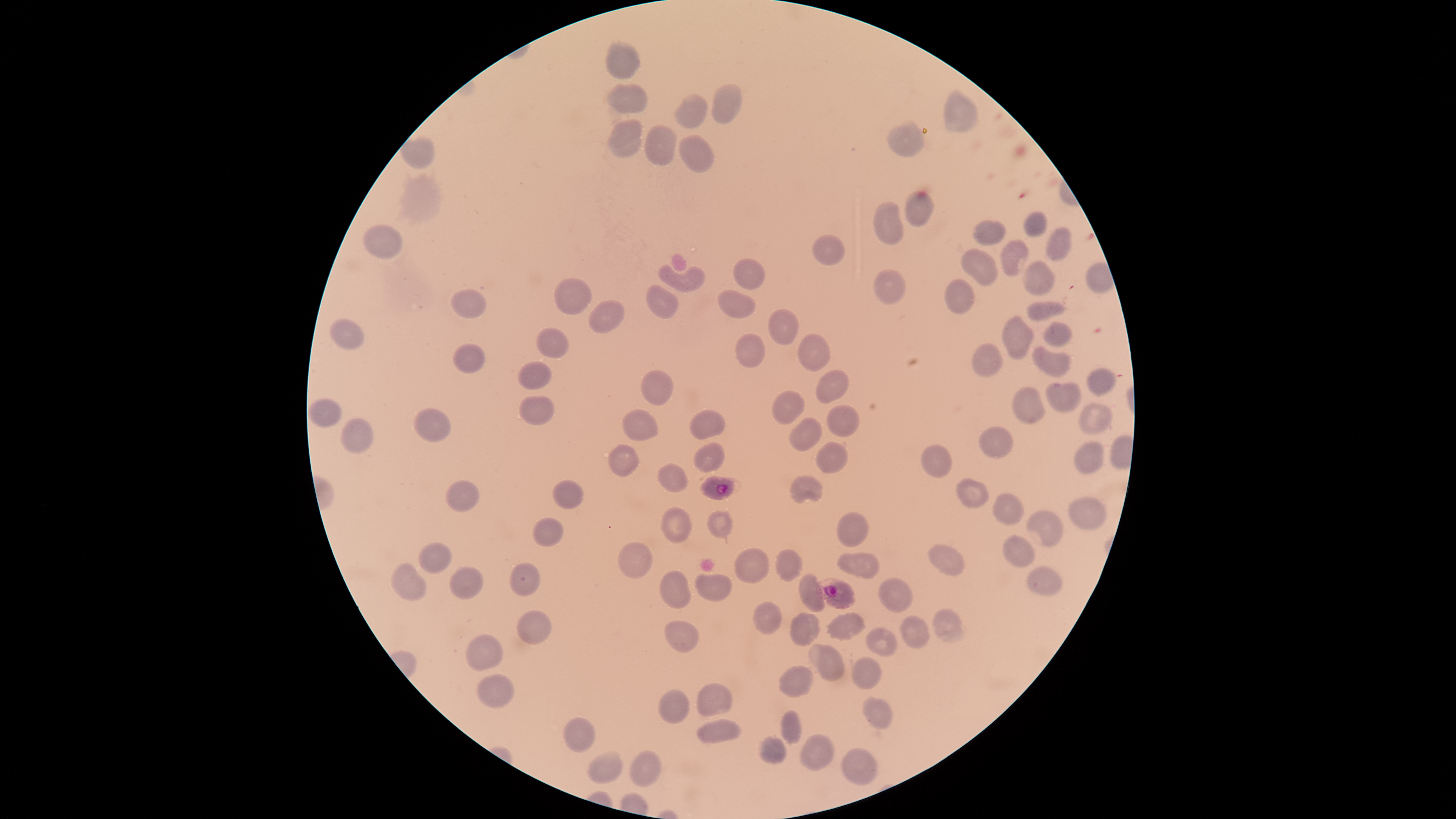

{
  "presence": "malaria parasites identified",
  "capture": "smartphone photograph through the microscope eyepiece",
  "image_size": "1456×819 pixels",
  "parasitized_RBCs": "approximate bounding boxes as {left, top, right, bottom} in pixels: {700, 476, 740, 500}, {815, 578, 855, 609}",
  "preparation": "thin smear of blood",
  "stain": "Giemsa",
  "species": "Plasmodium falciparum",
  "uninfected_RBCs": "approximate bounding boxes as {left, top, right, bottom} in pixels: {605, 39, 641, 78}, {607, 83, 649, 114}, {711, 83, 742, 125}, {944, 88, 979, 132}, {674, 94, 709, 129}, {607, 118, 644, 157}, {887, 120, 925, 158}, {644, 124, 676, 166}, {678, 134, 714, 174}, {399, 135, 436, 169}, {904, 190, 935, 227}, {872, 201, 905, 246}, {1023, 211, 1048, 238}, {972, 219, 1006, 246}, {361, 225, 404, 259}, {1045, 226, 1072, 261}, {811, 233, 847, 266}, {999, 238, 1028, 277}, {960, 247, 998, 288}, {732, 257, 767, 290}, {1022, 259, 1057, 296}, {657, 263, 706, 292}, {873, 269, 907, 305}, {553, 277, 592, 316}, {943, 278, 975, 314}, {645, 283, 679, 319}, {451, 289, 488, 318}, {716, 289, 757, 319}, {587, 299, 626, 334}, {1026, 300, 1068, 321}, {767, 308, 799, 346}, {1001, 314, 1035, 360}, {328, 318, 365, 350}, {1041, 321, 1072, 347}, {536, 326, 571, 359}, {734, 332, 766, 369}, {797, 332, 831, 372}, {971, 342, 1004, 377}, {452, 343, 486, 374}, {1031, 345, 1072, 377}, {517, 360, 551, 390}, {1087, 366, 1117, 397}, {641, 368, 674, 406}, {816, 370, 850, 405}, {1044, 381, 1081, 414}, {1011, 386, 1046, 424}, {771, 390, 805, 425}, {518, 395, 556, 426}, {308, 398, 342, 428}, {1077, 402, 1114, 436}, {826, 404, 861, 438}, {621, 407, 658, 442}, {413, 408, 453, 442}, {689, 409, 726, 440}, {788, 416, 823, 453}, {341, 418, 374, 454}, {977, 425, 1014, 459}, {815, 441, 848, 474}, {1074, 441, 1104, 473}, {692, 442, 725, 473}, {608, 443, 640, 477}, {920, 443, 953, 478}, {656, 462, 689, 493}, {790, 474, 824, 504}, {552, 477, 585, 509}, {955, 477, 990, 509}, {445, 479, 480, 512}, {992, 491, 1026, 525}, {1067, 496, 1109, 530}, {660, 505, 693, 545}, {706, 509, 733, 544}, {1026, 510, 1063, 546}, {836, 511, 870, 548}, {531, 516, 564, 547}, {1002, 534, 1036, 568}, {617, 541, 653, 579}, {417, 542, 453, 575}, {927, 543, 966, 575}, {734, 546, 770, 584}, {775, 548, 804, 582}, {837, 552, 881, 580}, {509, 561, 541, 597}, {390, 562, 427, 602}, {448, 566, 484, 600}, {1026, 566, 1063, 596}, {658, 570, 692, 610}, {797, 571, 826, 612}, {694, 572, 732, 602}, {878, 576, 912, 613}, {751, 600, 783, 635}, {931, 607, 965, 643}, {515, 608, 552, 646}, {789, 611, 822, 647}, {825, 611, 866, 641}, {898, 614, 930, 648}, {664, 619, 700, 653}, {865, 626, 898, 657}, {465, 633, 504, 673}, {808, 643, 845, 682}, {850, 656, 882, 691}, {778, 663, 814, 698}, {476, 674, 515, 709}, {696, 682, 733, 718}, {657, 689, 690, 725}, {864, 695, 894, 730}, {778, 709, 802, 746}, {563, 716, 596, 754}, {695, 718, 742, 744}, {799, 733, 835, 771}, {756, 735, 787, 764}, {840, 746, 878, 785}, {587, 750, 624, 784}, {629, 750, 661, 788}",
  "visible_region": "circular",
  "field_of_view": "single"
}